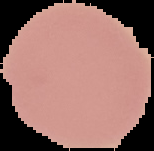

{
  "image_size": "154×151 pixels",
  "preparation": "thin blood film",
  "image_type": "cell region segmented out of the field of view; surrounding area masked to black",
  "malaria_status": "uninfected"
}